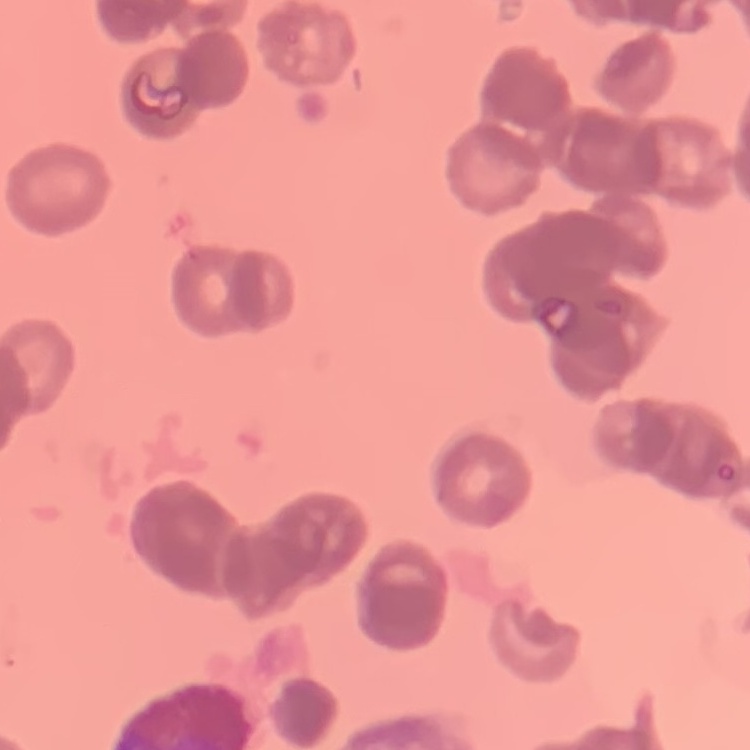
erythrocyte_morphology: rouleaux formation
image_type: one tile cut from a larger photomicrograph
stain: Field's or Giemsa
preparation: thin peripheral smear